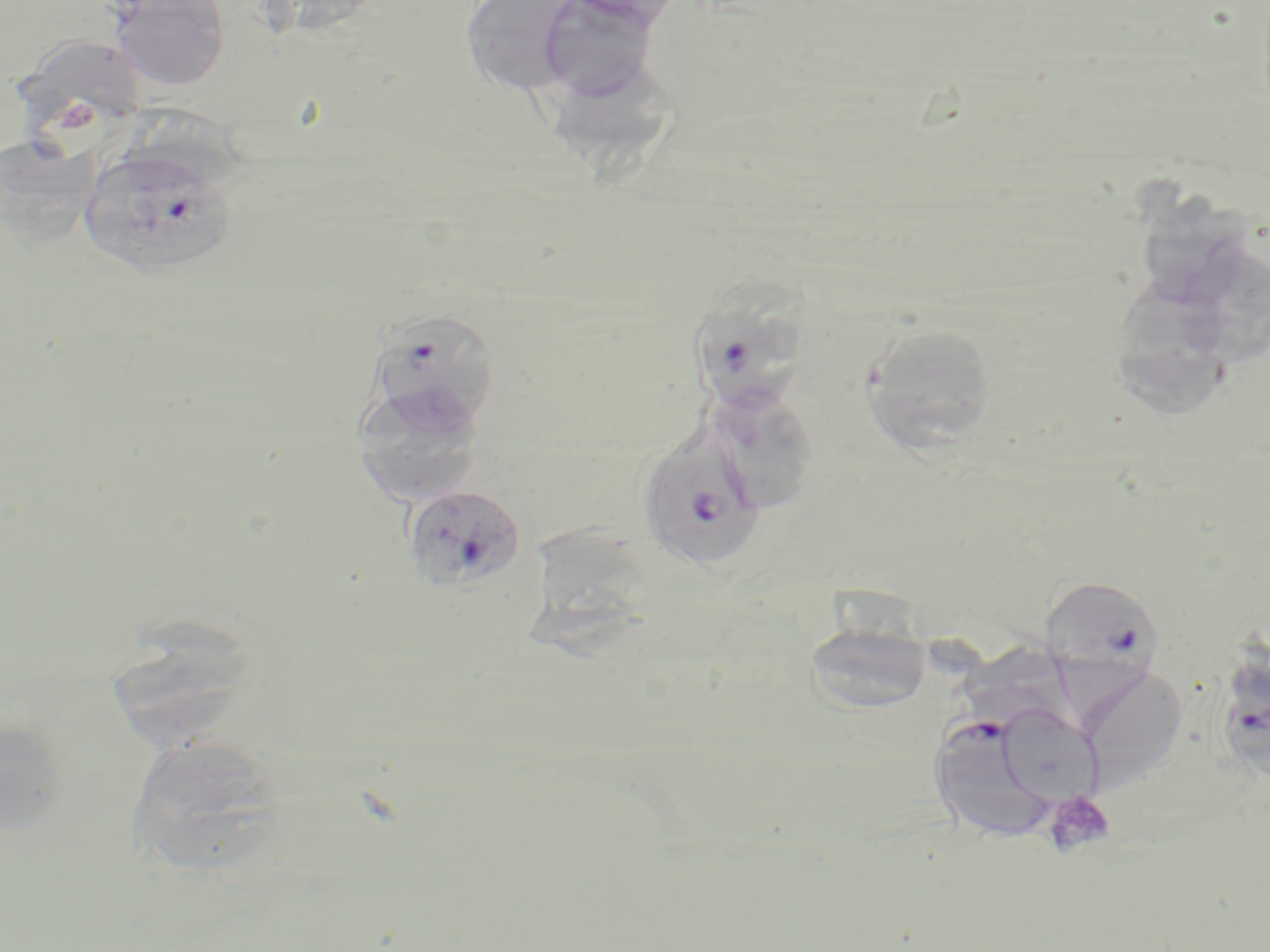

Summary:
  - Coordinate format: approximate bounding boxes as (x1, y1, x2, y2) in pixels
  - Uninfected red blood cell locations: (108, 0, 231, 92), (460, 0, 585, 98), (557, 0, 688, 28), (534, 1, 663, 104), (11, 33, 148, 136), (560, 65, 683, 182), (0, 133, 91, 254), (1135, 175, 1251, 301), (1171, 243, 1270, 368), (1118, 278, 1234, 417), (858, 323, 999, 455), (351, 382, 487, 507), (717, 392, 816, 513), (527, 524, 667, 661), (802, 619, 934, 716), (105, 620, 259, 752), (956, 632, 1079, 726), (1075, 663, 1188, 792), (993, 704, 1104, 806), (0, 711, 71, 841), (124, 741, 289, 875)
  - Plasmodium falciparum-infected red blood cell locations: (80, 147, 238, 279), (696, 278, 809, 424), (361, 309, 502, 439), (637, 434, 765, 572), (402, 483, 527, 594), (1039, 575, 1164, 680), (1219, 659, 1270, 773), (929, 719, 1047, 843)
  - Platelet locations: (59, 99, 101, 133), (1042, 789, 1116, 857)
  - Slide-level diagnosis: Plasmodium falciparum
  - Stain: May-Grünwald-Giemsa
  - Field of view: single
  - Image size: 1270×952 pixels
  - Modality: optical microscopy
  - Magnification: 1000x
  - Preparation: thin blood smear